Comment on the morphology of the erythrocytes.
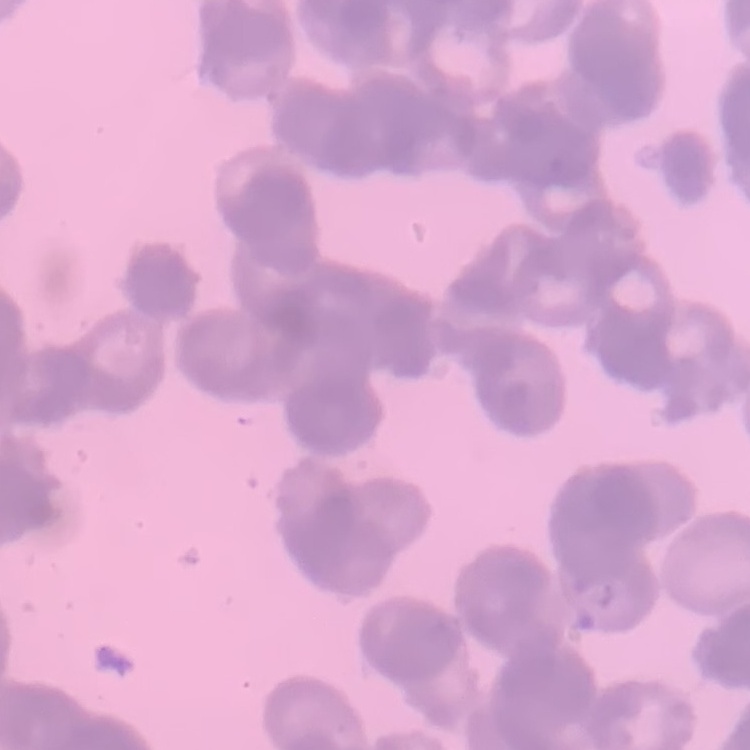

Rouleaux formation.

stain = Field's or Giemsa
image type = square crop of a larger photomicrograph
preparation = thin blood smear